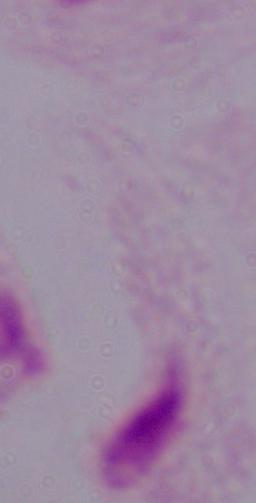 Photomicrograph. Captured at 1000x magnification. A trichomonad is seen.